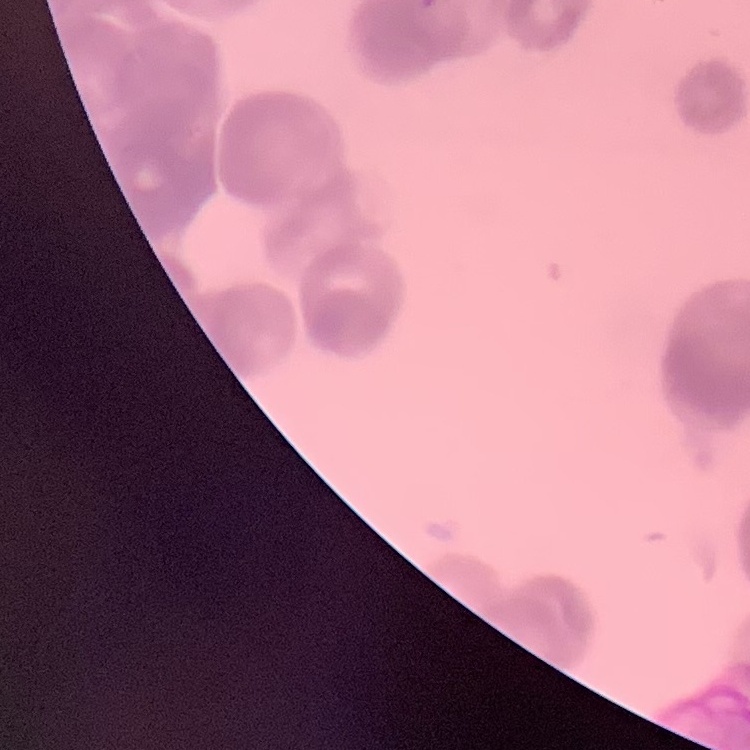
Summary:
  - Red blood cell morphology: rouleaux formation
  - Image type: one tile cut from a larger photomicrograph
  - Preparation: thin peripheral smear
  - Stain: Field's or Giemsa